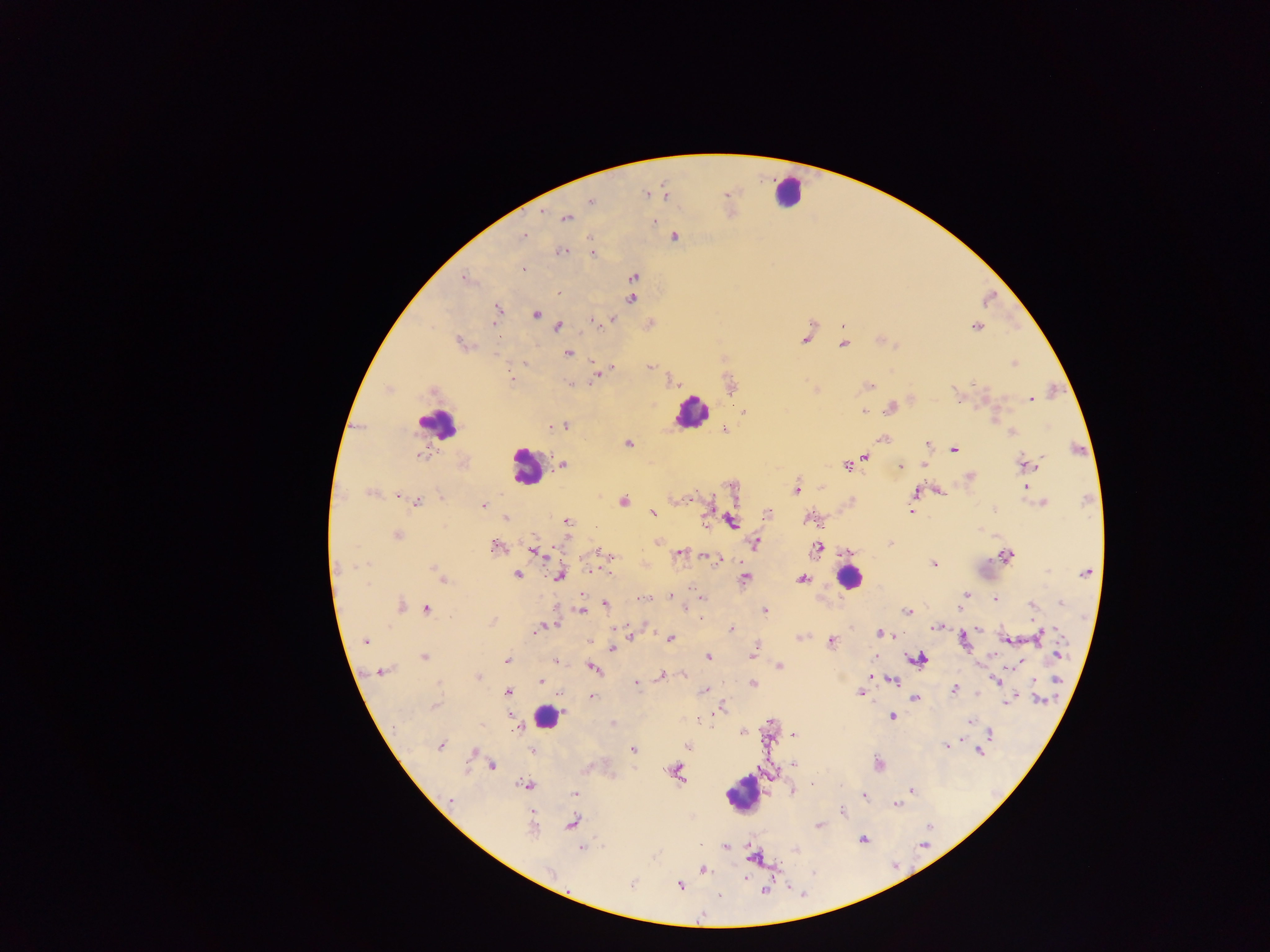
country: Ghana
capture: mobile-phone photograph through a microscope
image_size: 1270×952 pixels
leukocyte_locations: 'approximate centers as {x, y} in pixels: {788, 191}, {690, 411}, {437, 424}, {526, 466}, {849, 577}, {547, 716}, {742, 794}'
preparation: thick blood smear
field_of_view: single
malaria_parasite_locations: 'approximate centers as {x, y} in pixels: {646, 193}, {665, 196}, {591, 201}, {541, 212}, {565, 218}, {654, 221}, {524, 236}, {674, 237}, {590, 238}, {562, 252}, {592, 253}, {524, 270}, {633, 277}, {464, 278}, {558, 292}, {631, 298}, {498, 310}, {536, 314}, {613, 320}, {593, 321}, {493, 324}, {558, 326}, {976, 326}, {805, 338}, {460, 343}, {843, 344}, {568, 353}, {525, 363}, {1014, 363}, {594, 366}, {649, 367}, {613, 368}, {595, 378}, {511, 380}, {570, 383}, {869, 386}, {1031, 399}, {891, 407}, {864, 411}, {566, 426}, {552, 427}, {725, 431}, {1013, 432}, {883, 438}, {628, 444}, {927, 444}, {955, 449}, {422, 455}, {865, 457}, {562, 464}, {1025, 464}, {924, 465}, {847, 466}, {900, 466}, {969, 477}, {1027, 487}, {796, 489}, {941, 491}, {369, 493}, {916, 493}, {399, 495}, {440, 497}, {691, 498}, {418, 501}, {624, 501}, {1043, 503}, {484, 506}, {911, 510}, {652, 513}, {767, 514}, {505, 517}, {808, 519}, {704, 520}, {567, 521}, {731, 521}, {397, 536}, {657, 542}, {755, 543}, {891, 543}, {496, 547}, {817, 548}, {534, 551}, {600, 552}, {679, 554}, {1005, 555}, {708, 557}, {716, 560}, {365, 564}, {934, 564}, {434, 568}, {438, 573}, {1086, 573}, {517, 575}, {560, 576}, {442, 578}, {744, 578}, {802, 579}, {965, 595}, {669, 596}, {701, 597}, {643, 599}, {995, 600}, {1061, 603}, {605, 604}, {400, 606}, {1032, 606}, {426, 609}, {581, 610}, {765, 611}, {907, 612}, {702, 618}, {492, 621}, {554, 625}, {936, 627}, {732, 628}, {980, 629}, {536, 632}, {881, 633}, {631, 636}, {1039, 636}, {799, 637}, {671, 639}, {1005, 639}, {590, 640}, {832, 641}, {964, 641}, {365, 642}, {756, 645}, {612, 649}, {754, 651}, {1059, 654}, {752, 656}, {424, 657}, {709, 657}, {917, 658}, {506, 660}, {556, 662}, {1019, 662}, {779, 667}, {593, 668}, {381, 671}, {661, 676}, {683, 676}, {871, 676}, {478, 677}, {1057, 679}, {996, 681}, {541, 682}, {893, 682}, {636, 684}, {752, 684}, {705, 690}, {864, 690}, {954, 690}, {508, 692}, {860, 694}, {591, 696}, {916, 698}, {1040, 700}, {1007, 701}, {434, 705}, {719, 708}, {892, 716}, {969, 722}, {612, 724}, {516, 728}, {742, 733}, {989, 734}, {793, 735}, {441, 745}, {687, 746}, {947, 746}, {633, 749}, {532, 750}, {979, 752}, {473, 753}, {793, 764}, {492, 765}, {878, 765}, {678, 773}, {813, 783}, {525, 785}, {793, 790}, {911, 791}, {575, 793}, {863, 796}, {450, 800}, {897, 804}, {843, 811}, {573, 823}, {820, 826}, {532, 829}, {862, 839}, {725, 846}, {582, 848}, {795, 849}, {754, 858}, {703, 870}, {551, 873}, {632, 885}, {679, 886}, {766, 891}, {719, 895}'